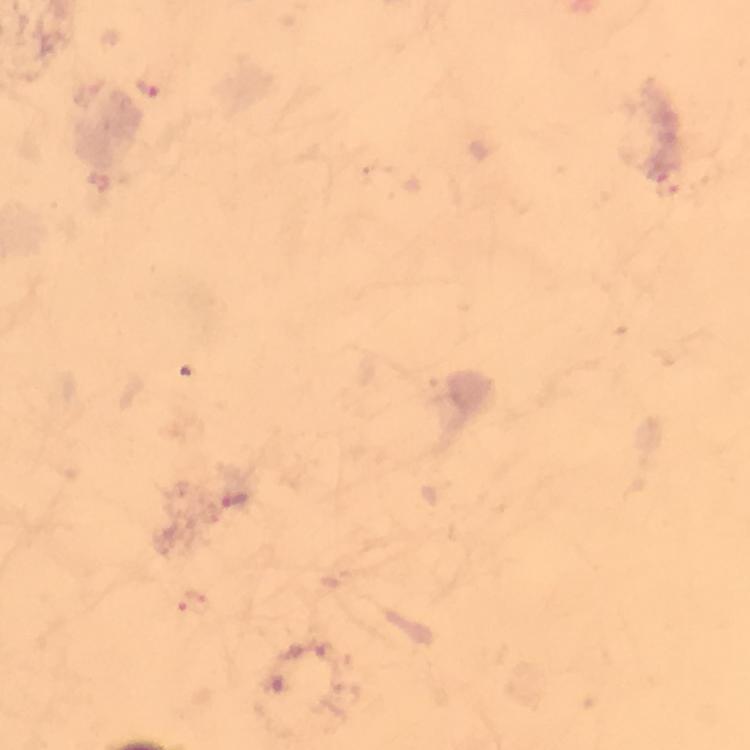
Approximate centers as {x, y} in pixels. Malaria parasite locations: {149, 87}, {669, 182}, {234, 499}, {194, 602}. Thick smear. A crop from one field of view. Immersion oil was used. Image is 750×750 pixels. From a malaria diagnostic workup. Giemsa-stained preparation. Smartphone photograph taken through a microscope. At 100x magnification.